Identify the preparation type.
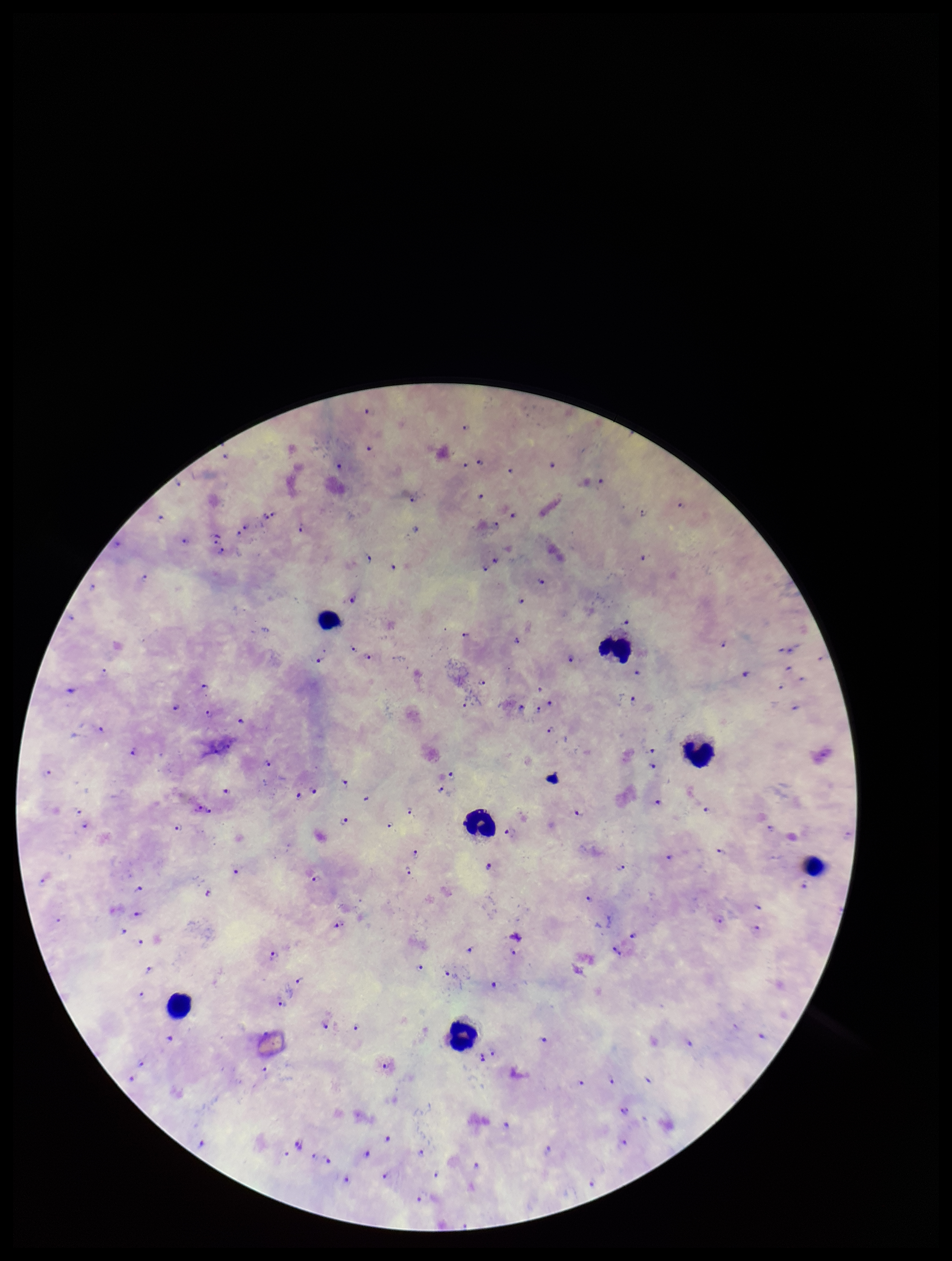
It is a thick blood smear.

capture: smartphone photograph through the microscope eyepiece
image_size: 952×1261 pixels
plasmodium_parasites: seen
patient_malaria_status: positive
leukocyte_count: 7
stain: Giemsa
species_reported_for_this_patient: Plasmodium falciparum
parasite_count: 85
field_of_view: single